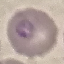

result: malaria parasites identified
preparation: thin smear
capture: smartphone through the microscope eyepiece
image_type: automatically extracted cell patch, resized to 64 × 64 pixels
stain: Giemsa